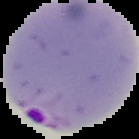 Malaria status: parasitized. The area outside the segmented cell region is set to black. From a thin blood film. Image is 139×139 pixels.